Identify the parasite.
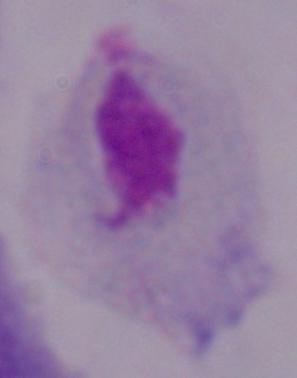
A trichomonad.

modality: micrograph
magnification: 1000x